Outline each blood parasite and name the species.
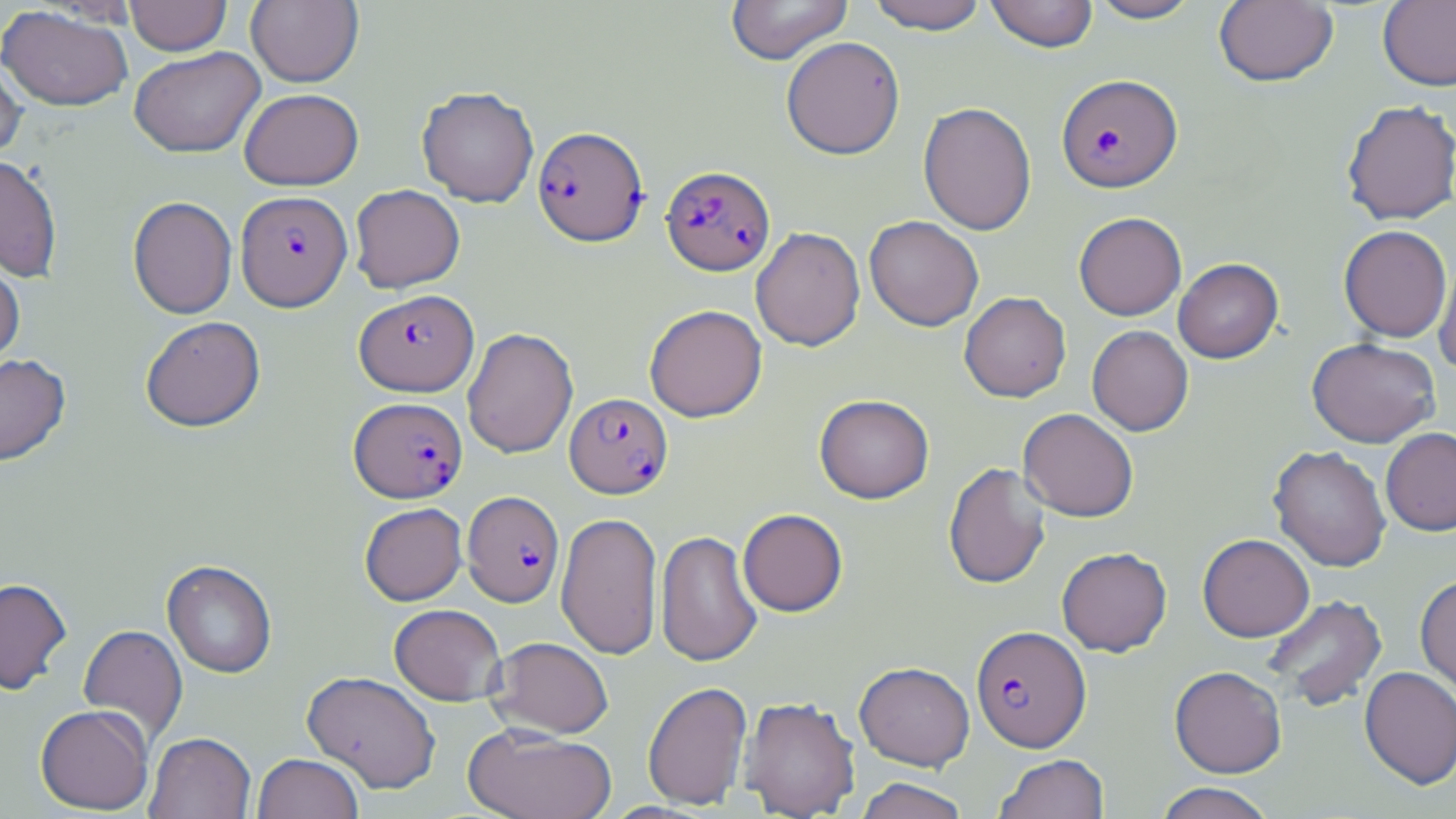
Approximate bounding boxes as [x1, y1, x2, y2] in pixels.
Plasmodium falciparum-infected red blood cells (subset): [1057, 74, 1182, 193], [532, 126, 649, 247], [661, 165, 775, 276], [238, 188, 355, 309], [565, 393, 673, 499], [349, 397, 468, 503], [462, 491, 564, 607], [971, 625, 1091, 752].
No Plasmodium ovale, Plasmodium malariae, Plasmodium vivax, Babesia divergens, or Trypanosoma brucei observed.

Uninfected red blood cell locations (subset): [124, 0, 232, 56], [725, 0, 853, 65], [866, 0, 989, 34], [984, 0, 1099, 52], [1087, 0, 1203, 23], [1214, 0, 1338, 87], [245, 1, 364, 87], [1378, 1, 1456, 91], [0, 5, 134, 112], [781, 36, 906, 159], [129, 46, 265, 158], [0, 53, 27, 163], [416, 86, 539, 207], [239, 88, 364, 190], [1340, 99, 1456, 225], [918, 101, 1037, 236], [0, 155, 63, 283], [349, 184, 465, 293], [128, 196, 237, 319], [1074, 212, 1187, 320], [864, 215, 984, 331], [1338, 225, 1452, 342], [750, 227, 866, 351], [0, 253, 25, 371], [1434, 253, 1456, 374], [1173, 258, 1283, 363], [959, 292, 1071, 402], [644, 304, 767, 422], [140, 315, 266, 432], [1087, 325, 1194, 436], [462, 327, 578, 458], [1307, 337, 1441, 447], [0, 354, 70, 466], [814, 394, 934, 503], [1018, 408, 1139, 522], [1381, 427, 1456, 536], [1269, 445, 1391, 572], [942, 462, 1051, 590], [359, 502, 467, 605], [737, 509, 848, 617], [556, 511, 663, 661], [655, 530, 763, 667], [1197, 533, 1314, 642], [1056, 547, 1172, 656], [162, 560, 277, 678], [1415, 574, 1456, 698], [0, 578, 72, 695], [1261, 594, 1388, 712], [389, 603, 506, 705], [78, 624, 187, 745], [487, 636, 614, 739], [854, 661, 975, 771], [1170, 666, 1287, 778], [1359, 666, 1456, 790], [301, 671, 441, 793], [642, 681, 753, 810], [739, 696, 861, 818], [35, 704, 154, 815], [463, 724, 617, 819], [145, 732, 255, 819], [252, 753, 364, 819], [993, 754, 1109, 819], [854, 777, 970, 819], [1153, 782, 1278, 819]. Slide-level diagnosis: Plasmodium falciparum. Light microscopy. Thin blood smear. Image is 1456×819 pixels. May-Grünwald-Giemsa stain. Single field of view. 1000x magnification.